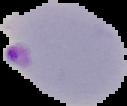 Result: Plasmodium parasites detected. Image is 127×106 pixels. From a thin blood film. Cell region segmented out of the field of view; the surrounding area is masked to black.